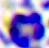
identification = white blood cell
magnification = 400x
modality = photomicrograph